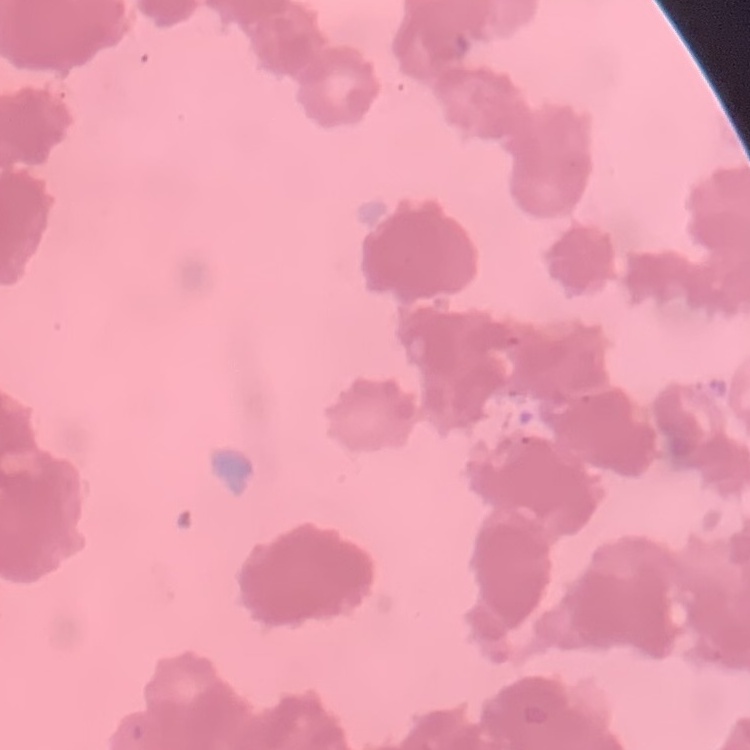

red blood cell morphology = rouleaux formation
image type = one tile cut from a larger photomicrograph
stain = Field's or Giemsa
preparation = thin peripheral smear